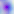

Summary:
  - Modality: micrograph
  - Identification: Toxoplasma gondii
  - Magnification: 400x